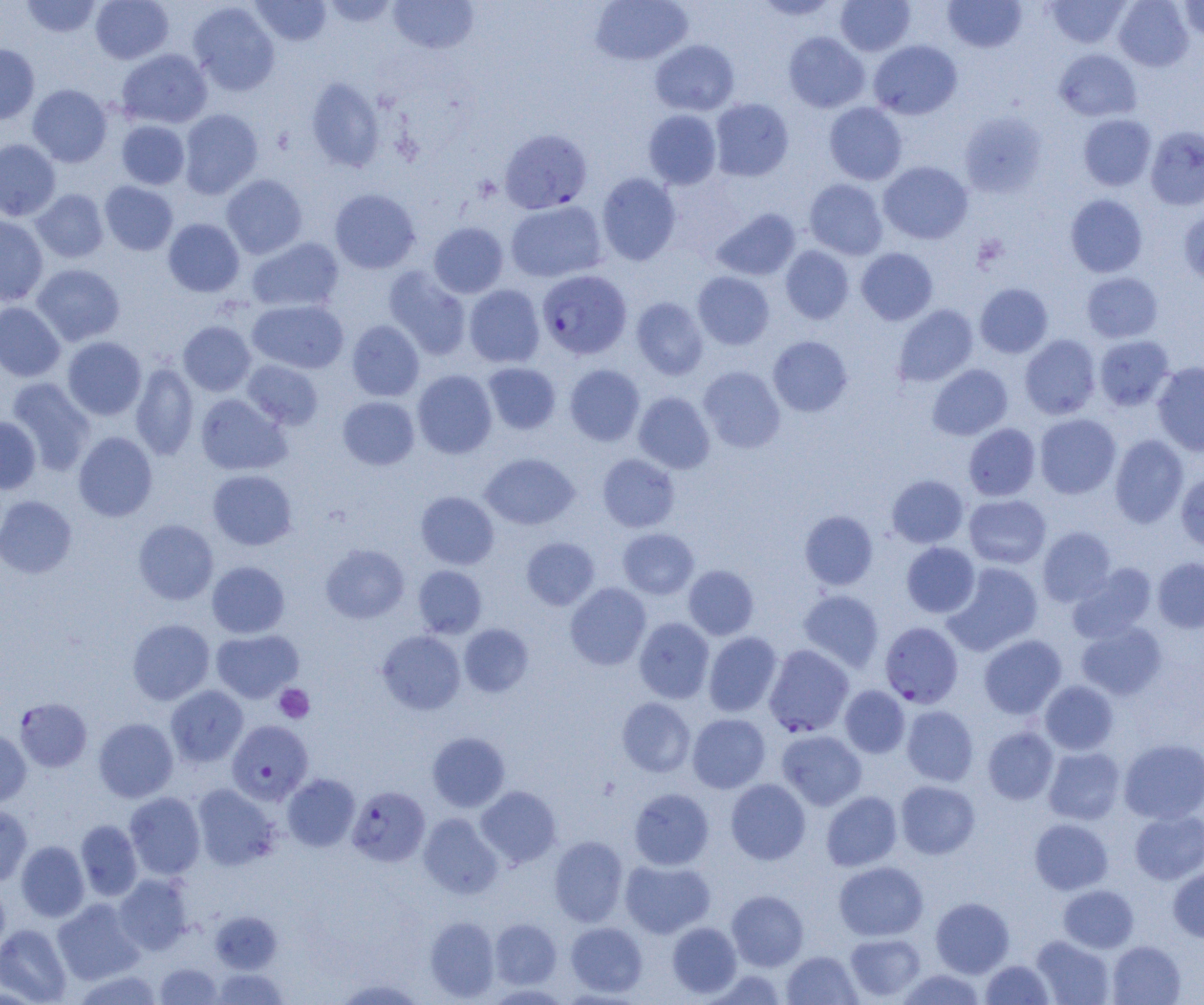
Summary:
  - Coordinate format: approximate bounding boxes as named x1/y1/x2/y2 corners in pixels
  - Uninfected red blood cell locations: (x1=21, y1=0, x2=103, y2=38), (x1=90, y1=0, x2=174, y2=64), (x1=250, y1=0, x2=332, y2=46), (x1=322, y1=0, x2=400, y2=28), (x1=387, y1=0, x2=479, y2=54), (x1=590, y1=0, x2=693, y2=66), (x1=753, y1=0, x2=842, y2=20), (x1=835, y1=0, x2=915, y2=56), (x1=1045, y1=0, x2=1130, y2=48), (x1=1113, y1=0, x2=1193, y2=71), (x1=1178, y1=0, x2=1204, y2=41), (x1=943, y1=1, x2=1026, y2=53), (x1=187, y1=2, x2=280, y2=95), (x1=783, y1=32, x2=870, y2=113), (x1=650, y1=40, x2=739, y2=116), (x1=868, y1=40, x2=962, y2=120), (x1=0, y1=44, x2=40, y2=124), (x1=116, y1=48, x2=213, y2=129), (x1=1054, y1=49, x2=1141, y2=122), (x1=305, y1=77, x2=384, y2=172), (x1=27, y1=84, x2=113, y2=167), (x1=709, y1=98, x2=794, y2=182), (x1=824, y1=102, x2=908, y2=185), (x1=178, y1=109, x2=263, y2=199), (x1=643, y1=109, x2=722, y2=189), (x1=959, y1=111, x2=1048, y2=198), (x1=1078, y1=114, x2=1156, y2=190), (x1=116, y1=120, x2=190, y2=189), (x1=1145, y1=126, x2=1204, y2=210), (x1=0, y1=139, x2=61, y2=221), (x1=879, y1=161, x2=973, y2=244), (x1=597, y1=172, x2=681, y2=265), (x1=221, y1=174, x2=308, y2=259), (x1=804, y1=179, x2=888, y2=259), (x1=100, y1=181, x2=178, y2=255), (x1=329, y1=188, x2=420, y2=274), (x1=31, y1=189, x2=109, y2=263), (x1=1065, y1=194, x2=1148, y2=277), (x1=505, y1=201, x2=606, y2=282), (x1=1179, y1=207, x2=1204, y2=285), (x1=711, y1=208, x2=801, y2=281), (x1=0, y1=215, x2=49, y2=306), (x1=162, y1=218, x2=245, y2=297), (x1=429, y1=222, x2=508, y2=298), (x1=247, y1=237, x2=344, y2=313), (x1=780, y1=246, x2=854, y2=324), (x1=856, y1=248, x2=938, y2=325), (x1=31, y1=263, x2=125, y2=346), (x1=383, y1=266, x2=471, y2=360), (x1=693, y1=271, x2=775, y2=350), (x1=1081, y1=272, x2=1163, y2=343), (x1=975, y1=283, x2=1053, y2=358), (x1=464, y1=284, x2=545, y2=368), (x1=631, y1=297, x2=708, y2=380), (x1=247, y1=299, x2=349, y2=374), (x1=0, y1=302, x2=66, y2=382), (x1=892, y1=304, x2=978, y2=387), (x1=178, y1=320, x2=256, y2=396), (x1=347, y1=320, x2=424, y2=401), (x1=1019, y1=335, x2=1101, y2=419), (x1=1094, y1=335, x2=1175, y2=411), (x1=768, y1=336, x2=852, y2=417), (x1=63, y1=337, x2=146, y2=420), (x1=242, y1=360, x2=323, y2=430), (x1=1152, y1=361, x2=1204, y2=456), (x1=131, y1=362, x2=199, y2=461), (x1=483, y1=363, x2=560, y2=434), (x1=564, y1=364, x2=645, y2=446), (x1=927, y1=364, x2=1013, y2=440), (x1=698, y1=367, x2=785, y2=453), (x1=412, y1=369, x2=497, y2=459), (x1=6, y1=377, x2=96, y2=475), (x1=634, y1=391, x2=715, y2=473), (x1=195, y1=393, x2=291, y2=475), (x1=337, y1=396, x2=420, y2=470), (x1=1034, y1=413, x2=1121, y2=499), (x1=0, y1=417, x2=41, y2=493), (x1=963, y1=423, x2=1041, y2=501), (x1=74, y1=432, x2=157, y2=521), (x1=1110, y1=434, x2=1189, y2=528), (x1=480, y1=453, x2=579, y2=530), (x1=597, y1=453, x2=680, y2=532), (x1=207, y1=469, x2=298, y2=550), (x1=1176, y1=472, x2=1204, y2=551), (x1=887, y1=474, x2=968, y2=548), (x1=415, y1=491, x2=499, y2=570), (x1=964, y1=495, x2=1051, y2=568), (x1=0, y1=496, x2=77, y2=578), (x1=800, y1=510, x2=878, y2=591), (x1=133, y1=519, x2=218, y2=605), (x1=1037, y1=526, x2=1117, y2=606), (x1=617, y1=528, x2=699, y2=599), (x1=521, y1=537, x2=600, y2=610), (x1=901, y1=542, x2=980, y2=618), (x1=320, y1=543, x2=409, y2=623), (x1=1152, y1=556, x2=1204, y2=633), (x1=207, y1=561, x2=290, y2=638), (x1=943, y1=563, x2=1043, y2=656), (x1=1067, y1=563, x2=1157, y2=643), (x1=413, y1=565, x2=487, y2=638), (x1=683, y1=565, x2=759, y2=640), (x1=565, y1=582, x2=651, y2=670), (x1=798, y1=589, x2=884, y2=672), (x1=634, y1=617, x2=714, y2=703), (x1=127, y1=619, x2=215, y2=705), (x1=1076, y1=621, x2=1166, y2=700), (x1=458, y1=623, x2=534, y2=697), (x1=211, y1=629, x2=303, y2=702), (x1=377, y1=630, x2=466, y2=715), (x1=703, y1=631, x2=782, y2=717), (x1=978, y1=634, x2=1067, y2=719), (x1=1040, y1=680, x2=1118, y2=755), (x1=840, y1=685, x2=910, y2=758), (x1=166, y1=686, x2=248, y2=767), (x1=617, y1=698, x2=695, y2=777), (x1=901, y1=705, x2=978, y2=786), (x1=687, y1=713, x2=770, y2=793), (x1=93, y1=718, x2=178, y2=802), (x1=983, y1=726, x2=1059, y2=804), (x1=0, y1=728, x2=31, y2=807), (x1=777, y1=729, x2=866, y2=810), (x1=427, y1=732, x2=510, y2=812), (x1=1119, y1=738, x2=1204, y2=824), (x1=1043, y1=747, x2=1125, y2=824), (x1=283, y1=773, x2=360, y2=852), (x1=725, y1=779, x2=811, y2=864), (x1=896, y1=780, x2=980, y2=858), (x1=192, y1=784, x2=280, y2=870), (x1=476, y1=785, x2=562, y2=868), (x1=629, y1=788, x2=714, y2=870), (x1=821, y1=791, x2=902, y2=871), (x1=124, y1=792, x2=205, y2=879), (x1=0, y1=803, x2=32, y2=886), (x1=1130, y1=810, x2=1204, y2=885), (x1=418, y1=813, x2=503, y2=898), (x1=1029, y1=818, x2=1113, y2=894), (x1=76, y1=819, x2=143, y2=901), (x1=549, y1=836, x2=628, y2=927), (x1=16, y1=840, x2=89, y2=921), (x1=620, y1=859, x2=715, y2=938), (x1=834, y1=861, x2=928, y2=941), (x1=1169, y1=864, x2=1204, y2=943), (x1=114, y1=874, x2=193, y2=955), (x1=0, y1=880, x2=10, y2=961), (x1=1058, y1=885, x2=1139, y2=953), (x1=727, y1=890, x2=808, y2=971), (x1=931, y1=897, x2=1014, y2=977), (x1=52, y1=898, x2=145, y2=984), (x1=210, y1=910, x2=283, y2=973), (x1=425, y1=916, x2=500, y2=1001), (x1=490, y1=918, x2=561, y2=989), (x1=566, y1=922, x2=648, y2=996), (x1=667, y1=922, x2=742, y2=997), (x1=0, y1=923, x2=71, y2=1005), (x1=845, y1=933, x2=926, y2=1001), (x1=1031, y1=935, x2=1115, y2=1005), (x1=1107, y1=940, x2=1186, y2=1005), (x1=782, y1=951, x2=861, y2=1004), (x1=981, y1=959, x2=1054, y2=1004), (x1=154, y1=963, x2=222, y2=1004), (x1=213, y1=968, x2=287, y2=1005), (x1=72, y1=969, x2=165, y2=1004), (x1=706, y1=969, x2=788, y2=1004), (x1=899, y1=969, x2=986, y2=1005), (x1=334, y1=977, x2=426, y2=1004)
  - Platelet locations: (x1=973, y1=234, x2=1008, y2=270), (x1=274, y1=684, x2=314, y2=723)
  - Plasmodium falciparum-infected red blood cell locations: (x1=499, y1=128, x2=592, y2=214), (x1=537, y1=270, x2=632, y2=359), (x1=880, y1=621, x2=963, y2=708), (x1=764, y1=644, x2=854, y2=736), (x1=16, y1=697, x2=92, y2=773), (x1=227, y1=720, x2=313, y2=804), (x1=346, y1=786, x2=430, y2=867)
  - Slide-level diagnosis: Plasmodium falciparum
  - Field of view: single
  - Magnification: 1000x
  - Image size: 1204×1005 pixels
  - Modality: light microscopy
  - Preparation: thin blood film